Assess for Plasmodium parasites.
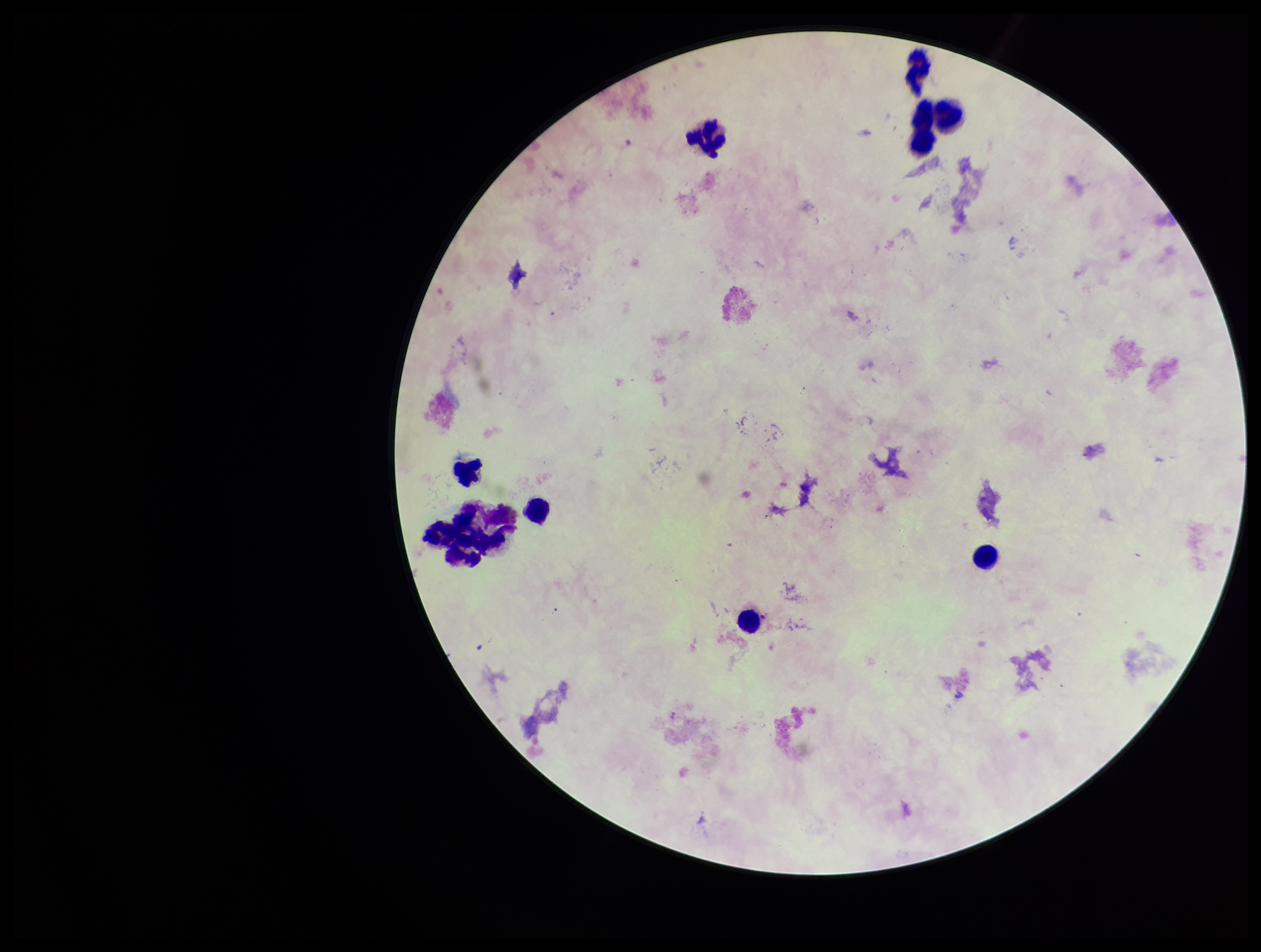

None identified.

patient malaria status = positive
stain = Giemsa
leukocyte count = 10
parasite count = 0
preparation = thick
image size = 1261×952 pixels
field of view = single
capture = smartphone photograph through the microscope eyepiece
species reported for this patient = Plasmodium falciparum